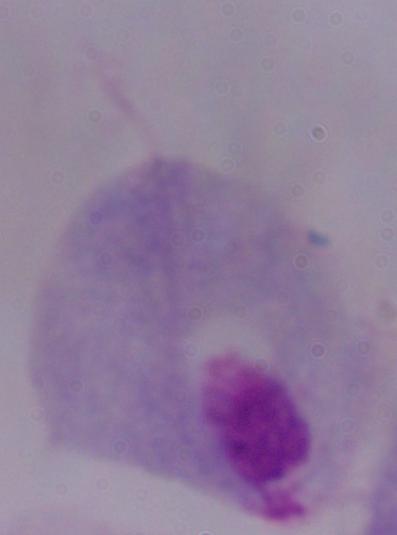

Summary:
  - Magnification: 1000x
  - Identification: trichomonad
  - Modality: photomicrograph